Point out every malaria parasite.
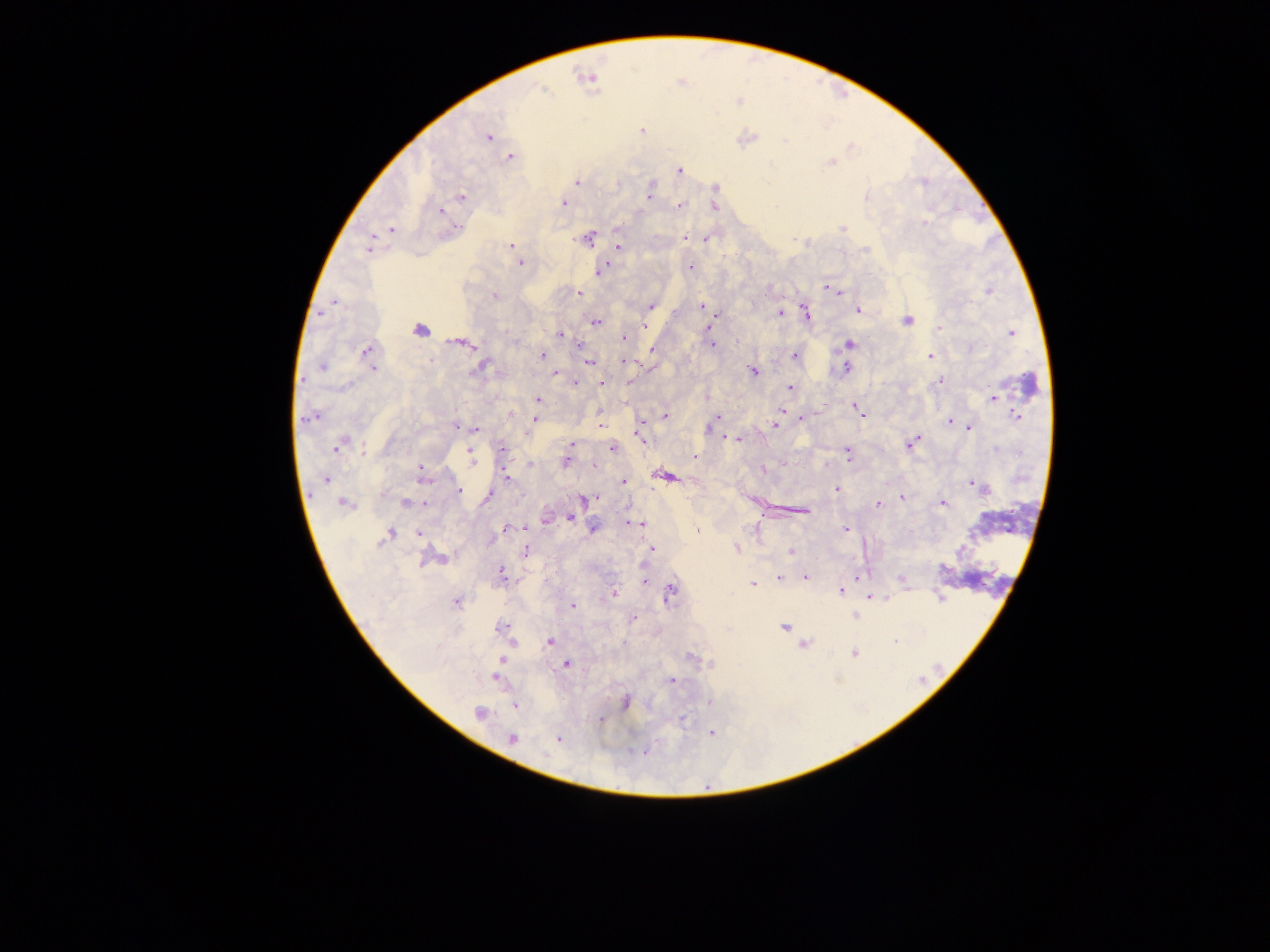
Approximate centers as [x, y] in pixels.
Malaria parasites: [543, 92], [487, 137], [783, 139], [509, 157], [679, 170], [576, 181], [648, 193], [462, 196], [563, 202], [679, 204], [437, 210], [925, 223], [392, 229], [845, 229], [686, 235], [589, 236], [705, 241], [511, 245], [617, 246], [368, 248], [864, 250], [520, 262], [691, 265], [601, 271], [826, 288], [577, 291], [987, 291], [580, 293], [495, 297], [332, 301], [701, 305], [652, 306], [805, 310], [861, 312], [322, 313], [781, 313], [718, 315], [907, 321], [596, 322], [712, 323], [645, 327], [707, 327], [419, 329], [938, 329], [1011, 332], [560, 335], [622, 339], [446, 341], [458, 343], [468, 344], [712, 344], [848, 344], [368, 349], [652, 351], [795, 354], [543, 355], [930, 356], [623, 361], [590, 362], [845, 368], [478, 369], [374, 370], [753, 372], [555, 374], [940, 381], [576, 382], [600, 383], [629, 383], [789, 387], [993, 399], [537, 401], [855, 406], [783, 410], [1018, 414], [717, 416], [801, 416], [808, 416], [862, 416], [664, 417], [315, 418], [303, 419], [535, 419], [948, 421], [599, 422], [711, 424], [454, 425], [772, 425], [709, 427], [969, 428], [476, 430], [640, 435], [917, 436], [733, 439], [743, 439], [726, 440], [739, 440], [348, 441], [339, 444], [571, 444], [911, 444], [337, 447], [613, 448], [907, 448], [472, 451], [848, 453], [362, 454], [694, 457], [566, 460], [472, 462], [593, 463], [529, 464], [422, 465], [765, 469], [662, 476], [506, 478], [668, 479], [329, 481], [624, 481], [426, 482], [971, 484], [837, 488], [460, 491], [487, 497], [597, 497], [901, 497], [583, 499], [590, 499], [343, 502], [877, 503], [943, 503], [405, 504], [806, 513], [568, 519], [544, 520], [634, 523], [640, 525], [505, 527], [591, 527], [846, 529], [697, 530], [418, 533], [390, 535], [491, 543], [380, 545], [737, 548], [653, 549], [527, 550], [790, 552], [441, 558], [427, 559], [502, 572], [856, 575], [780, 577], [805, 577], [645, 582], [902, 582], [752, 583], [841, 592], [614, 593], [938, 597], [869, 599], [457, 602], [574, 606], [855, 615], [634, 620], [497, 628], [784, 628], [551, 641], [511, 642], [803, 645], [503, 659], [567, 664], [496, 679], [671, 679], [626, 701], [515, 706], [480, 714], [512, 740], [644, 750].

field of view = single
country = Ghana
preparation = thick blood smear
capture = mobile-phone photograph through a microscope
image size = 1270×952 pixels